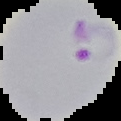

Cell region segmented out of the field of view; the surrounding area is masked to black. Result: Plasmodium parasites identified. From a thin blood smear. Image is 121×121 pixels.